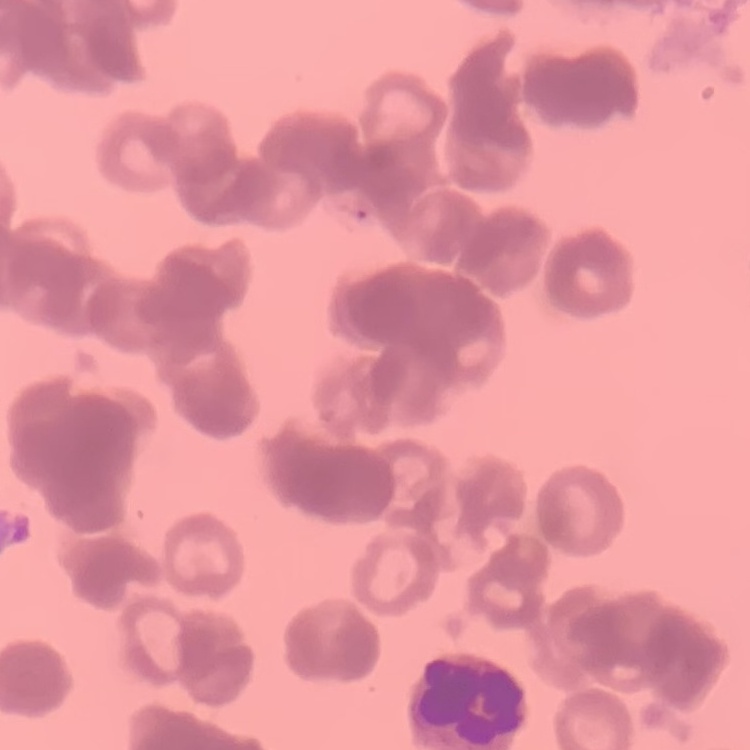

Summary:
  - Erythrocyte morphology: rouleaux formation
  - Preparation: thin peripheral smear
  - Stain: Field's or Giemsa
  - Image type: square crop of a larger photomicrograph